State which cell type is depicted.
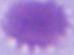

An erythrocyte.

Summary:
  - Magnification: 1000x
  - Modality: photomicrograph